Report the malaria status of this cell.
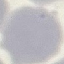

It is uninfected.

Thin blood film. Acquired by smartphone through the microscope eyepiece. Cell patch, automatically extracted from a larger field of view and resized to 64 × 64 pixels. Giemsa-stained preparation.